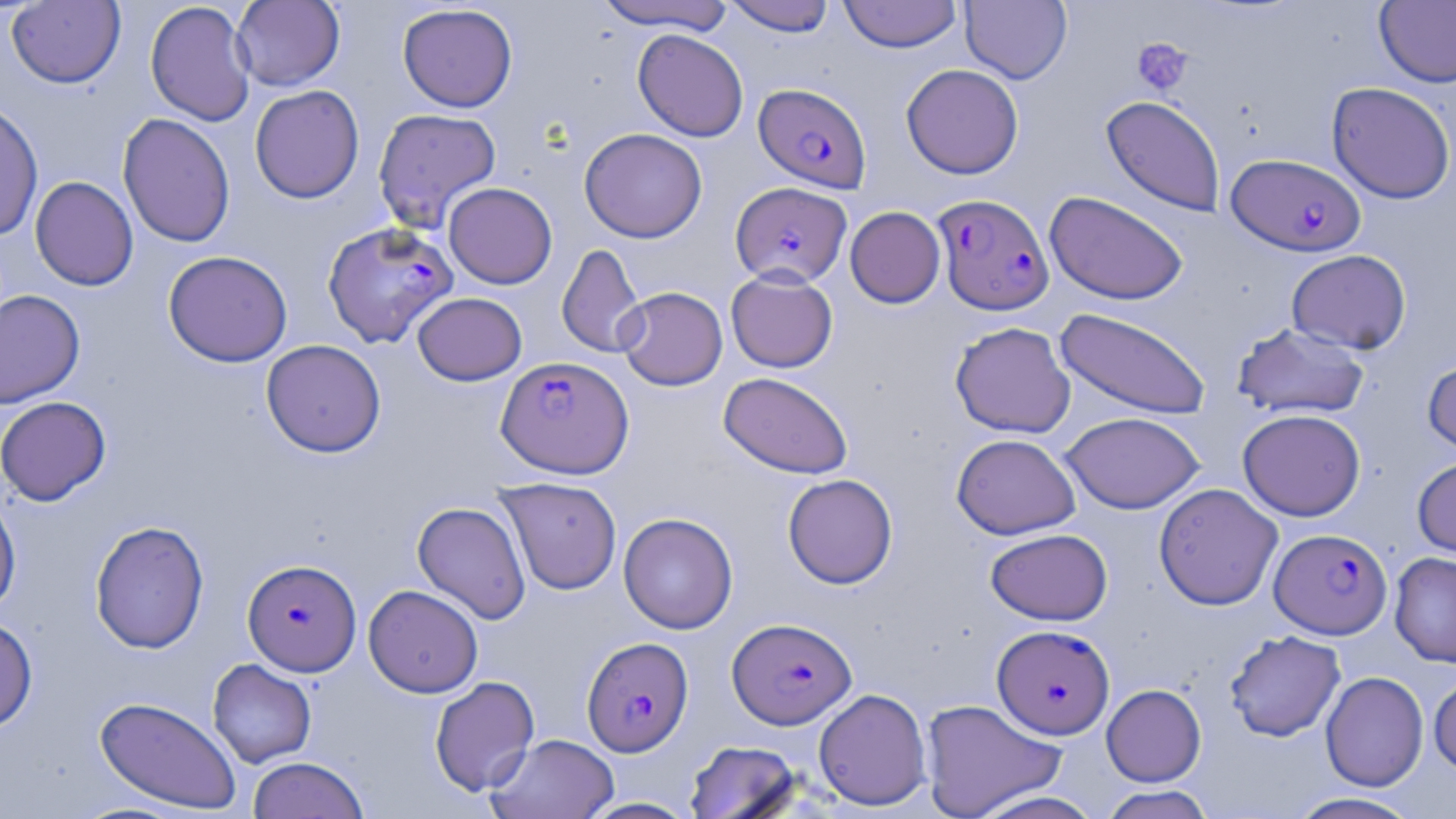
Summary:
  - Coordinate format: approximate bounding boxes as [x1, y1, x2, y2] in pixels
  - Platelet locations: [1132, 37, 1193, 95]
  - Plasmodium falciparum-infected red blood cell locations: [753, 82, 872, 192], [1226, 153, 1365, 256], [731, 182, 851, 287], [933, 193, 1054, 315], [322, 222, 459, 348], [496, 355, 635, 478], [1270, 528, 1392, 639], [243, 558, 362, 675], [728, 617, 856, 728], [992, 624, 1114, 739], [582, 636, 693, 756]
  - Uninfected red blood cell locations: [231, 0, 345, 91], [723, 0, 836, 36], [838, 0, 962, 53], [960, 0, 1072, 84], [6, 1, 126, 89], [145, 1, 256, 126], [591, 1, 735, 34], [1374, 1, 1456, 88], [397, 3, 518, 112], [632, 28, 749, 142], [901, 64, 1023, 179], [1326, 82, 1455, 204], [249, 84, 365, 204], [1101, 95, 1226, 217], [0, 99, 43, 241], [373, 108, 502, 233], [118, 113, 236, 247], [580, 127, 707, 243], [30, 176, 138, 291], [443, 182, 557, 288], [1044, 191, 1189, 305], [845, 206, 946, 308], [557, 243, 646, 358], [1286, 249, 1411, 354], [163, 250, 293, 367], [725, 269, 838, 373], [615, 286, 728, 391], [0, 289, 85, 409], [412, 292, 527, 386], [1054, 308, 1213, 420], [950, 321, 1076, 438], [1232, 322, 1370, 420], [261, 339, 386, 457], [1422, 356, 1456, 459], [718, 371, 853, 479], [0, 396, 112, 506], [1237, 408, 1366, 520], [1060, 411, 1206, 514], [951, 433, 1080, 539], [1412, 455, 1456, 560], [783, 473, 897, 589], [494, 477, 622, 595], [1153, 482, 1283, 610], [0, 489, 21, 620], [412, 501, 531, 624], [618, 512, 738, 634], [90, 520, 209, 654], [985, 528, 1112, 625], [1389, 551, 1456, 667], [363, 584, 483, 698], [0, 616, 38, 733], [1224, 630, 1346, 741], [207, 658, 317, 768], [1320, 670, 1429, 792], [1428, 674, 1456, 774], [429, 675, 540, 796], [1101, 684, 1206, 786], [813, 688, 932, 810], [95, 696, 242, 814], [919, 698, 1065, 819], [486, 733, 619, 819], [685, 740, 803, 819], [247, 756, 369, 819], [1100, 785, 1215, 819], [968, 789, 1105, 819], [1286, 792, 1425, 818], [576, 797, 700, 818]
  - Slide-level diagnosis: Plasmodium falciparum
  - Magnification: 1000x
  - Field of view: single
  - Stain: May-Grünwald-Giemsa
  - Modality: optical microscopy
  - Image size: 1456×819 pixels
  - Preparation: thin blood film